Assess this cell for malaria.
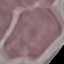
It is uninfected.

preparation = thin blood smear
stain = Giemsa
capture = smartphone camera at the microscope eyepiece
image type = cell patch, automatically extracted from a larger field of view and resized to 64 × 64 pixels